Report the malaria status of this cell.
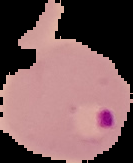
Parasitized.

The area outside the segmented cell region is set to black. Image is 133×163 pixels. From a thin blood film.